Outline each Babesia divergens-infected red blood cell.
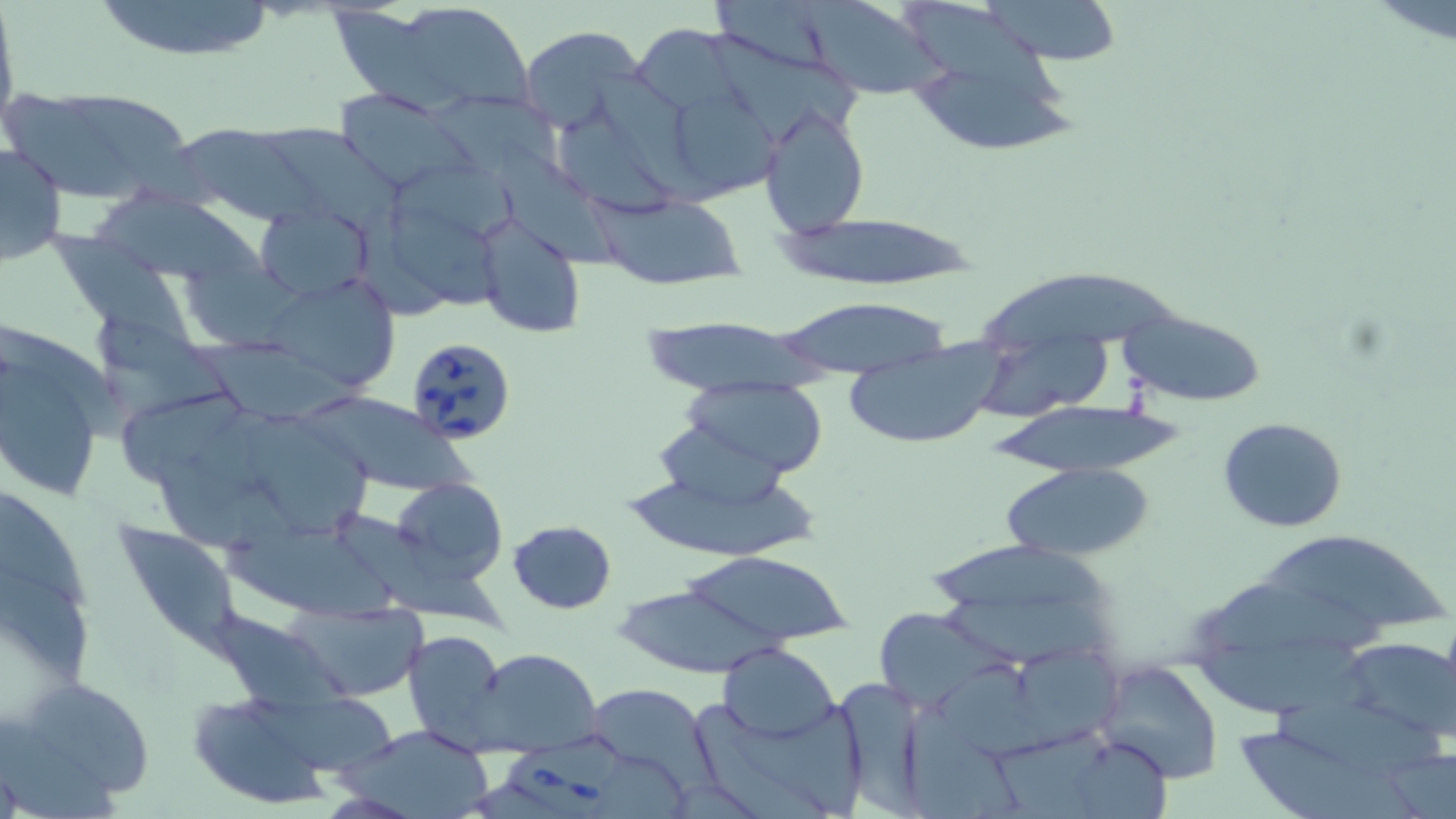
Approximate bounding boxes as (x1, y1, x2, y2) in pixels.
Babesia divergens-infected red blood cells: (405, 336, 517, 445), (506, 736, 615, 819).

Summary:
  - Uninfected red blood cell locations: (90, 0, 281, 62), (797, 0, 947, 101), (974, 0, 1125, 64), (907, 1, 1066, 106), (331, 7, 474, 117), (402, 7, 540, 109), (632, 22, 739, 110), (901, 25, 1082, 160), (520, 26, 642, 132), (710, 33, 862, 139), (67, 89, 228, 211), (337, 90, 473, 193), (5, 97, 149, 200), (679, 98, 793, 199), (757, 104, 869, 235), (557, 118, 684, 220), (178, 123, 328, 227), (268, 126, 409, 230), (0, 142, 68, 267), (500, 145, 625, 272), (400, 165, 521, 240), (99, 192, 275, 278), (589, 194, 746, 288), (257, 203, 374, 298), (391, 206, 518, 315), (774, 213, 983, 287), (473, 214, 587, 340), (44, 229, 180, 340), (978, 260, 1182, 347), (271, 283, 401, 391), (769, 296, 957, 376), (1118, 311, 1266, 408), (1, 325, 114, 504), (973, 334, 1112, 418), (183, 341, 374, 428), (842, 344, 1007, 449), (681, 376, 831, 477), (123, 394, 244, 490), (308, 396, 485, 495), (987, 399, 1179, 476), (1218, 416, 1348, 532), (654, 417, 799, 508), (256, 419, 370, 537), (617, 458, 819, 563), (1004, 463, 1153, 561), (390, 475, 509, 588), (0, 494, 92, 612), (339, 512, 511, 638), (507, 521, 616, 613), (220, 525, 414, 629), (116, 529, 250, 665), (1265, 533, 1450, 631), (930, 535, 1112, 616), (675, 548, 853, 650), (0, 572, 92, 691), (1193, 574, 1396, 658), (613, 583, 783, 677), (930, 589, 1125, 668), (291, 602, 425, 701), (880, 605, 1017, 708), (215, 610, 361, 712), (1199, 628, 1381, 714), (403, 630, 509, 751), (1340, 636, 1456, 744), (718, 643, 839, 742), (476, 648, 603, 755), (1022, 649, 1136, 738), (1095, 660, 1225, 785), (11, 675, 156, 806), (833, 675, 933, 815), (247, 683, 406, 777), (586, 683, 714, 788), (187, 691, 336, 809), (1272, 693, 1443, 776), (750, 696, 865, 816), (695, 702, 843, 819), (904, 703, 1026, 819), (1239, 722, 1413, 819), (342, 726, 498, 819), (997, 733, 1102, 819), (1076, 738, 1182, 819)
  - Slide-level diagnosis: Babesia divergens
  - Field of view: one of a larger specimen
  - Magnification: 1000x
  - Preparation: thin blood film
  - Stain: May-Grünwald-Giemsa
  - Image size: 1456×819 pixels
  - Modality: optical microscopy